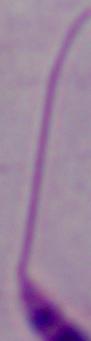

modality = micrograph
identification = Leishmania
magnification = 1000x